Assess this cell for malaria.
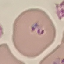
Parasitized.

Thin smear of blood. Cell patch, automatically extracted from a larger field of view and resized to 64 × 64 pixels. Giemsa-stained preparation. Acquired by smartphone through the microscope eyepiece.